Assess the morphology of the erythrocytes.
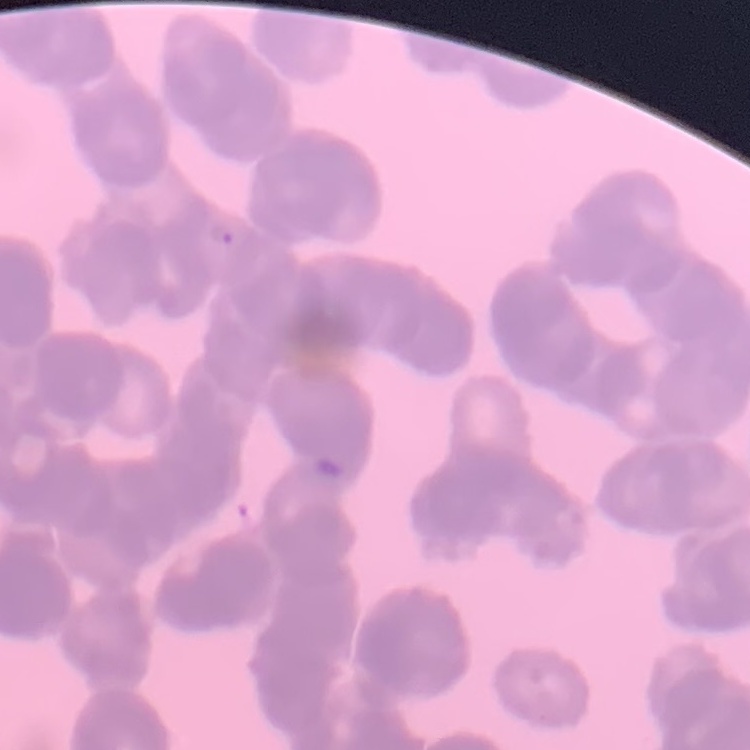
Rouleaux formation.

preparation = thin blood smear
stain = Field's or Giemsa
image type = one tile cut from a larger photomicrograph